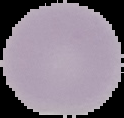
preparation = thin blood film
result = no Plasmodium parasites seen
image type = segmented cell region on a black background
image size = 124×118 pixels